Assess this cell for malaria.
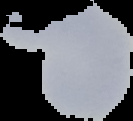

Uninfected.

Summary:
  - Image type: segmented cell region with the area outside set to black
  - Preparation: thin blood smear
  - Image size: 133×121 pixels